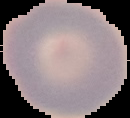

Malaria status: uninfected. From a thin blood film. Image is 130×118 pixels. Segmented cell region on a black background.